Comment on the morphology of the red blood cells.
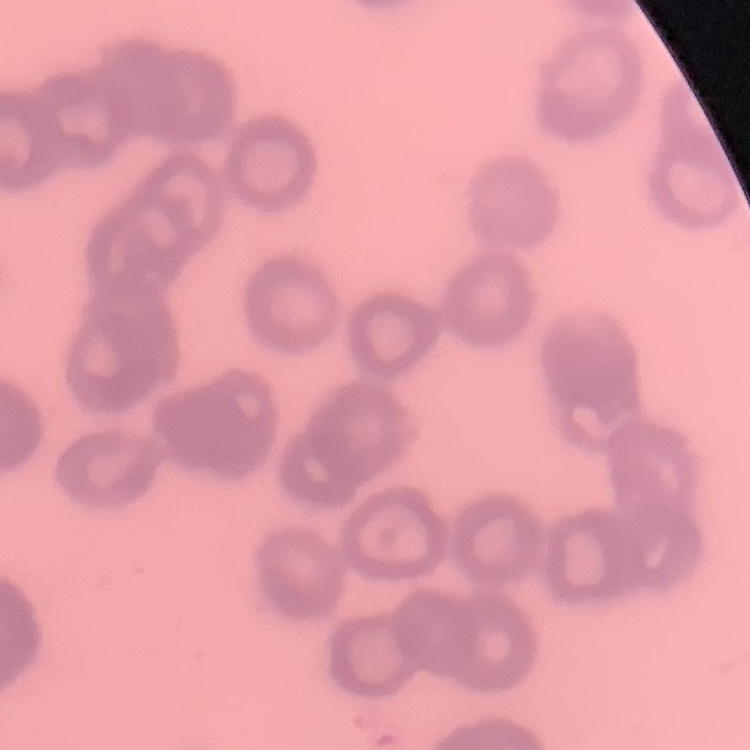

Rouleaux formation.

{
  "stain": "Field's or Giemsa",
  "image_type": "square crop of a larger photomicrograph",
  "preparation": "thin blood film"
}